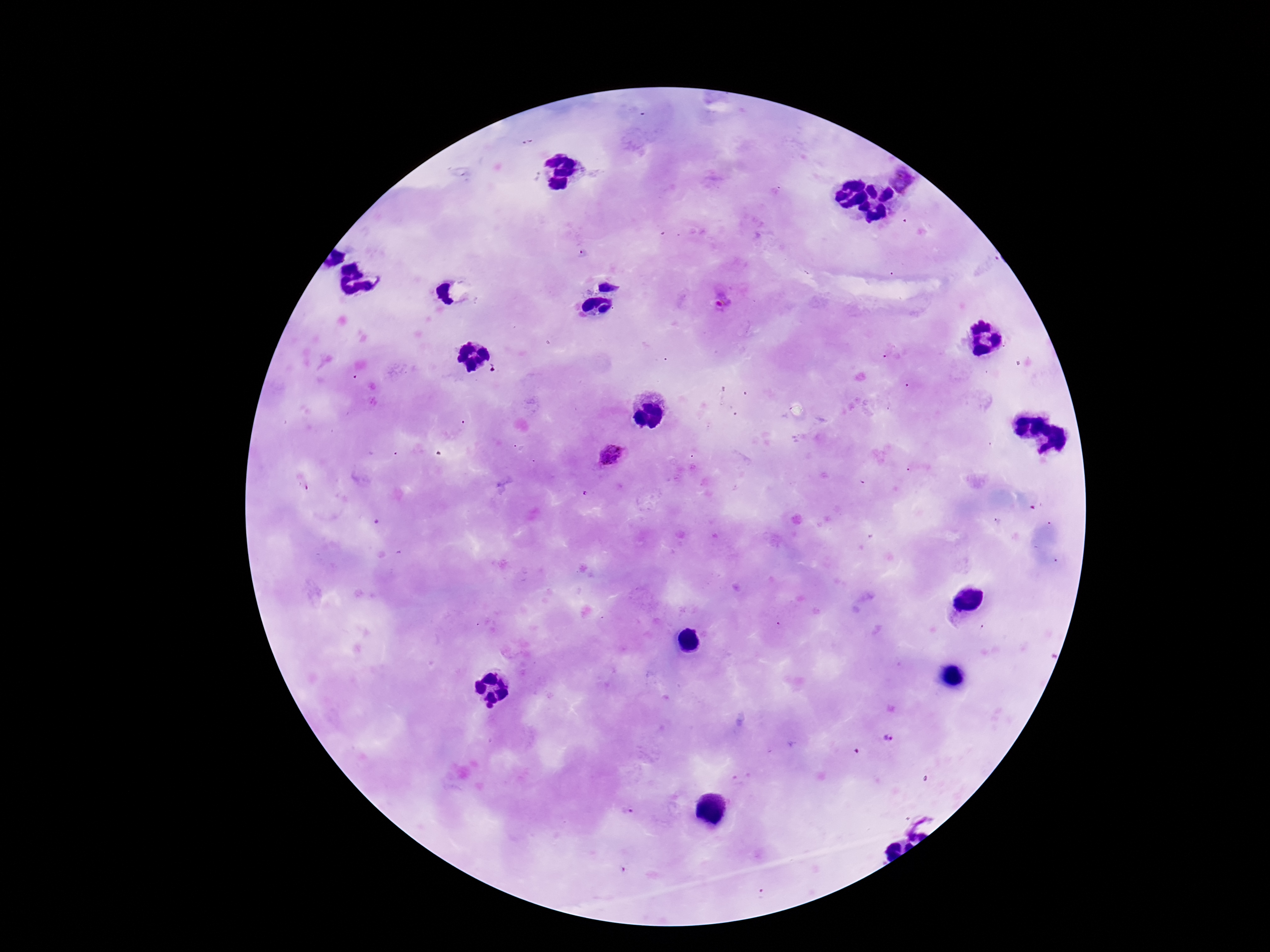
Approximate centers as {x, y} in pixels. Plasmodium parasite locations: {901, 179}, {721, 302}, {612, 454}, {490, 707}, {887, 739}, {915, 817}. Giemsa-stained preparation. Image is 1270×952 pixels. 100x magnification. Thick blood film. Single field of view. Patient malaria status: infected. Photographed through the microscope eyepiece with a smartphone camera.